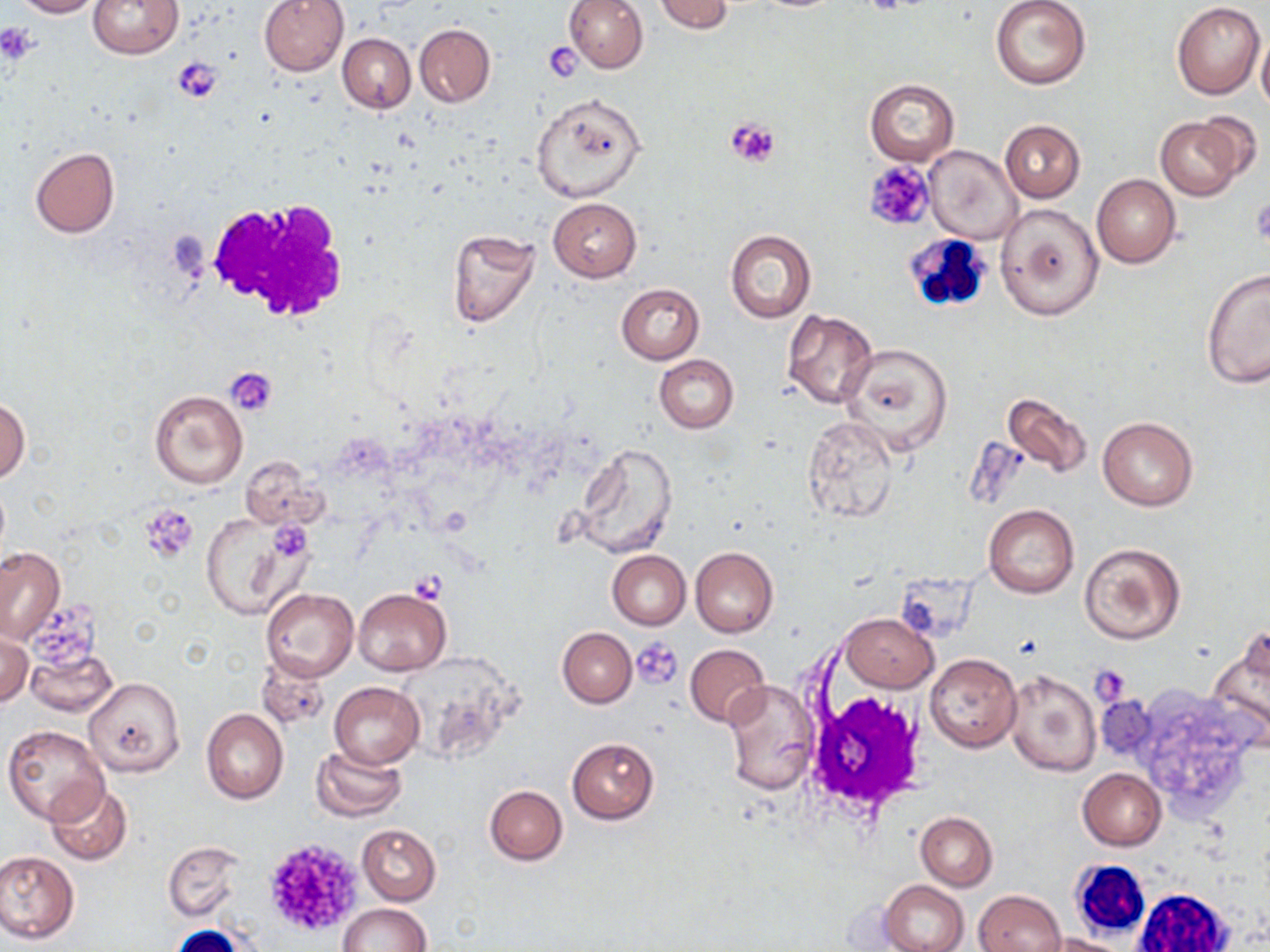

Summary:
  - Coordinate format: approximate bounding boxes as [x1, y1, x2, y2] in pixels
  - Uninfected red blood cell locations: [11, 0, 101, 18], [87, 0, 183, 58], [258, 0, 350, 76], [564, 0, 647, 73], [654, 0, 734, 34], [990, 0, 1091, 89], [1172, 3, 1265, 99], [414, 24, 495, 106], [339, 34, 415, 113], [1256, 34, 1270, 114], [864, 79, 959, 165], [530, 93, 647, 203], [1188, 111, 1264, 183], [1156, 116, 1243, 200], [999, 120, 1086, 203], [925, 146, 1022, 244], [29, 148, 119, 238], [1092, 174, 1182, 268], [548, 198, 641, 281], [994, 202, 1104, 322], [446, 229, 542, 329], [724, 229, 817, 324], [1201, 267, 1270, 387], [616, 283, 705, 364], [782, 309, 878, 410], [839, 341, 957, 455], [654, 355, 737, 432], [149, 390, 247, 489], [1002, 390, 1092, 478], [0, 394, 30, 484], [801, 416, 899, 523], [1098, 417, 1198, 512], [570, 444, 677, 560], [239, 457, 326, 530], [983, 504, 1079, 598], [200, 511, 298, 617], [1078, 542, 1186, 644], [0, 546, 64, 642], [690, 547, 778, 637], [606, 551, 689, 629], [262, 588, 359, 681], [353, 588, 450, 675], [841, 613, 938, 692], [558, 627, 637, 708], [1206, 629, 1270, 741], [0, 630, 32, 708], [686, 644, 770, 728], [26, 646, 117, 717], [924, 653, 1022, 753], [256, 656, 329, 730], [1004, 670, 1100, 776], [84, 677, 185, 777], [721, 679, 819, 794], [329, 681, 425, 768], [202, 710, 288, 804], [3, 724, 110, 824], [566, 738, 659, 823], [310, 745, 409, 822], [1077, 768, 1166, 851], [45, 783, 135, 866], [485, 785, 568, 864], [916, 812, 998, 889], [357, 823, 441, 905], [163, 840, 243, 921], [0, 850, 79, 943], [881, 879, 969, 952], [975, 889, 1065, 952], [339, 903, 432, 952], [1042, 934, 1131, 952]
  - Platelet locations: [0, 24, 40, 64], [542, 43, 581, 80], [173, 57, 223, 102], [724, 116, 780, 167], [863, 160, 936, 233], [1249, 198, 1269, 243], [226, 366, 279, 417], [139, 505, 198, 563], [270, 523, 311, 561], [409, 571, 449, 602], [29, 600, 112, 669], [632, 638, 684, 689], [1090, 666, 1132, 705], [261, 837, 363, 938]
  - White blood cell locations: [204, 197, 350, 323], [900, 232, 995, 318], [800, 686, 930, 823], [1067, 861, 1151, 943], [1129, 884, 1238, 952]
  - Slide-level diagnosis: no evidence of blood parasites
  - Field of view: single
  - Stain: May-Grünwald-Giemsa
  - Preparation: thin blood film
  - Image size: 1270×952 pixels
  - Modality: optical microscopy
  - Magnification: 1000x